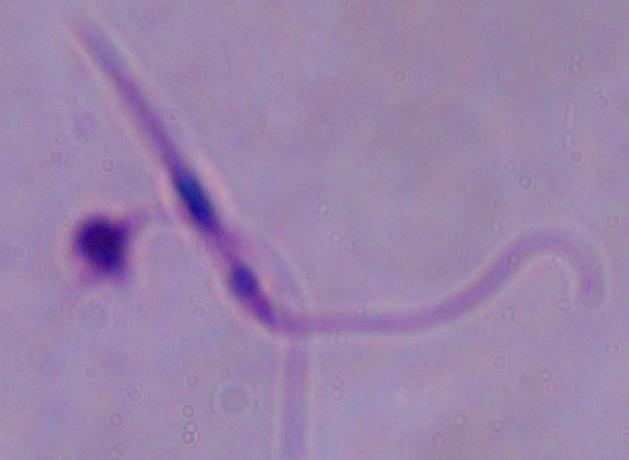

A Leishmania parasite is shown. Photomicrograph. Captured at 1000x magnification.